Locate every Plasmodium ovale-infected red blood cell.
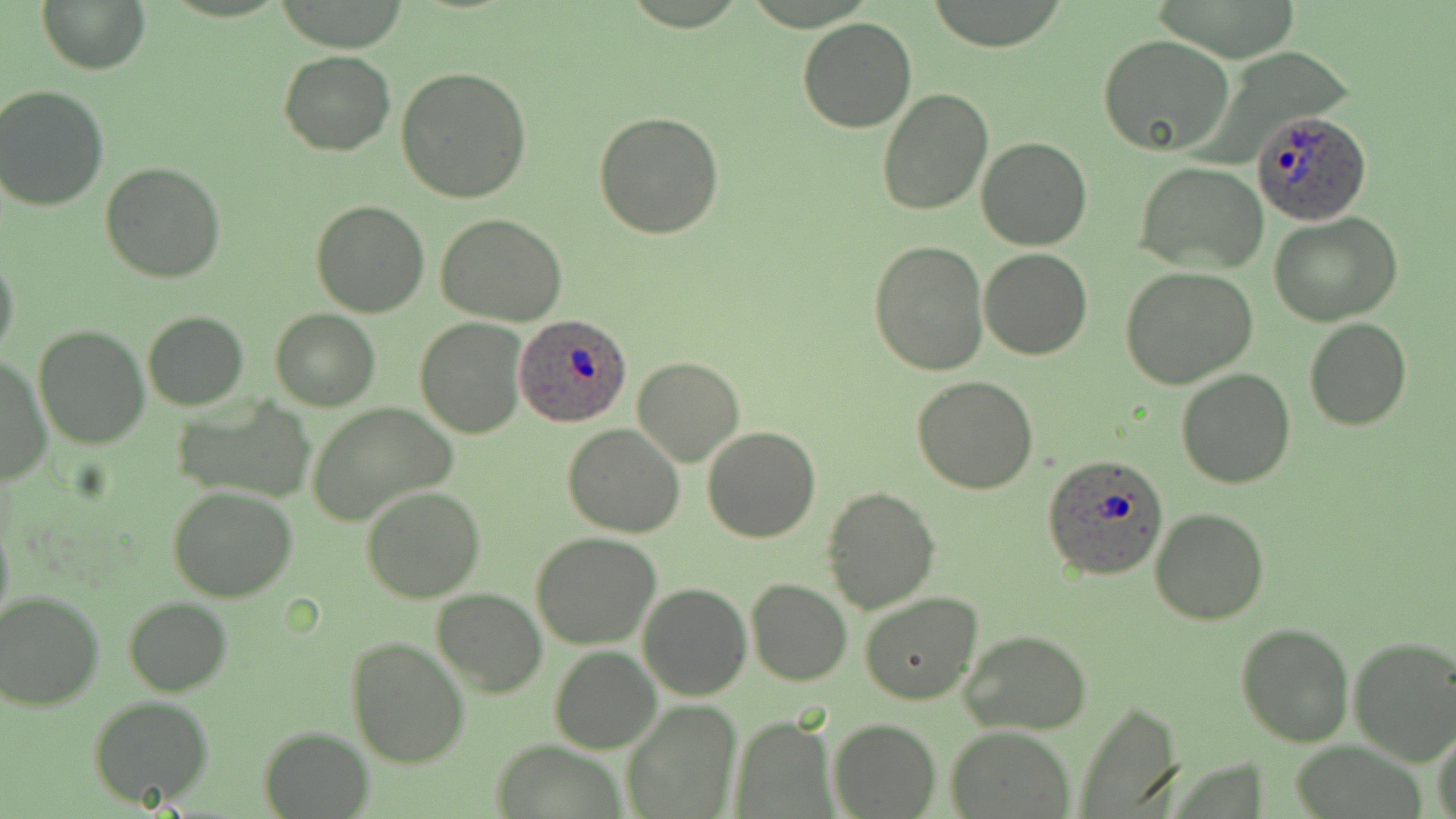

Approximate bounding boxes as (x1,y1)-(x2,y2) corner pairs in pixels.
Plasmodium ovale-infected red blood cells: (1251,109)-(1372,226), (514,311)-(631,426), (1044,453)-(1171,580).

Summary:
  - Uninfected red blood cell locations: (37,0)-(151,73), (796,18)-(918,133), (1097,34)-(1236,159), (279,52)-(396,154), (396,65)-(532,204), (2,84)-(112,210), (876,89)-(992,216), (593,111)-(723,240), (977,136)-(1091,251), (100,162)-(228,282), (1134,162)-(1269,274), (312,199)-(430,318), (1268,212)-(1404,328), (436,214)-(568,327), (868,238)-(991,376), (979,249)-(1093,360), (0,251)-(20,365), (1120,266)-(1260,387), (270,309)-(380,411), (142,311)-(249,411), (414,319)-(526,438), (1303,319)-(1411,432), (33,324)-(152,448), (631,357)-(745,467), (1,358)-(50,485), (1176,368)-(1296,489), (912,374)-(1039,494), (174,397)-(314,504), (310,402)-(455,524), (563,422)-(685,537), (701,427)-(821,544), (168,486)-(297,602), (361,487)-(485,603), (822,487)-(939,612), (1150,506)-(1269,625), (0,515)-(14,634), (532,532)-(661,648), (745,579)-(852,686), (639,582)-(751,700), (431,587)-(547,697), (0,589)-(104,709), (859,593)-(983,705), (124,597)-(231,695), (1236,623)-(1355,747), (961,630)-(1093,735), (346,635)-(470,770), (1348,636)-(1456,765), (549,645)-(661,753), (88,695)-(214,807), (621,699)-(743,819), (1075,699)-(1185,818), (734,716)-(833,816), (828,717)-(940,817), (1431,722)-(1456,819), (945,725)-(1075,818), (258,726)-(372,817)
  - Slide-level diagnosis: Plasmodium ovale
  - Preparation: thin blood film
  - Field of view: single
  - Modality: light microscopy
  - Stain: May-Grünwald-Giemsa
  - Image size: 1456×819 pixels
  - Magnification: 1000x